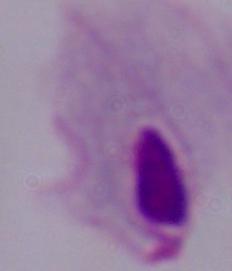

magnification = 1000x
modality = photomicrograph
identification = trichomonad